Outline each blood parasite and name the species.
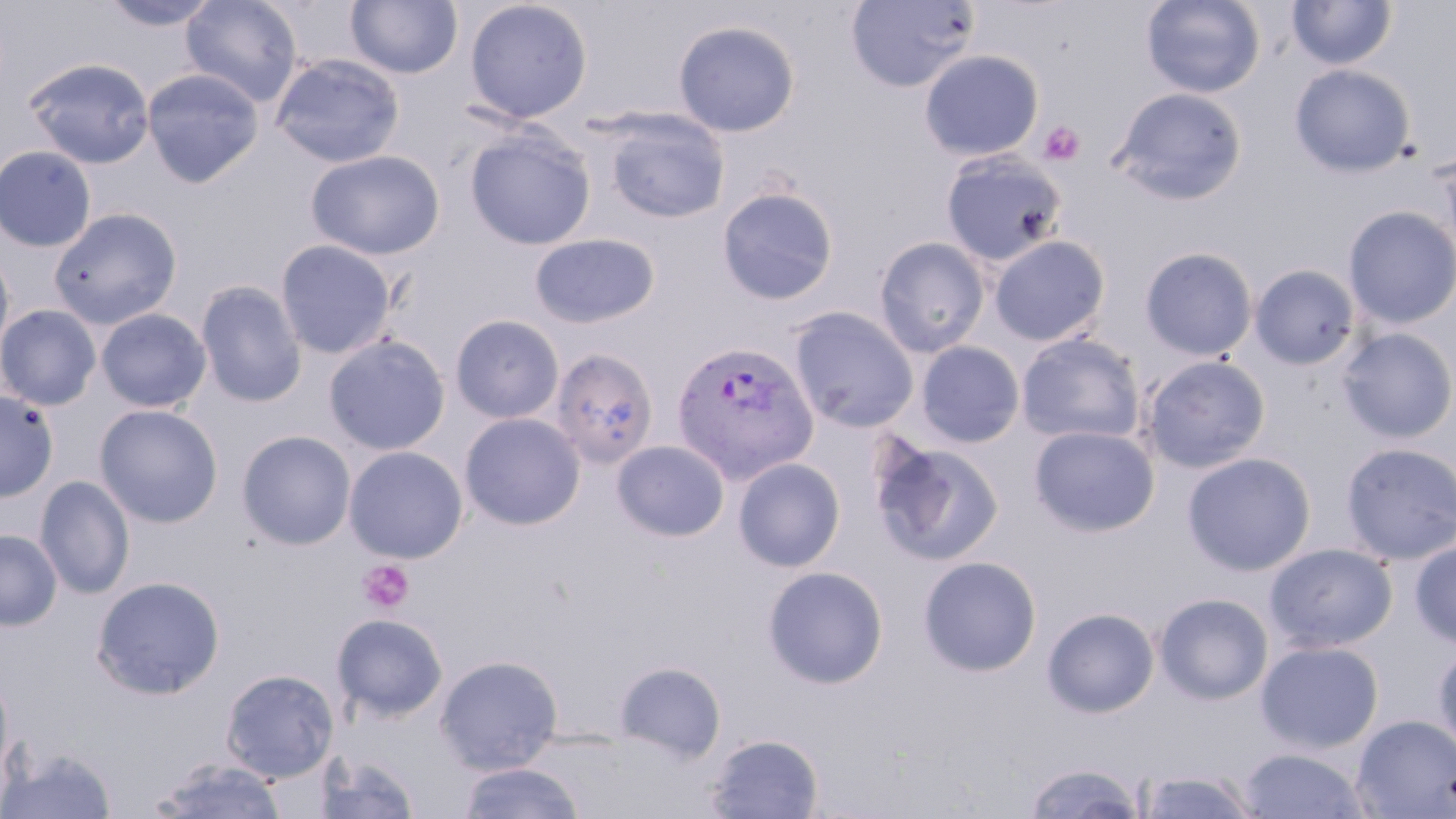
Approximate bounding boxes as [x1, y1, x2, y2] in pixels.
Plasmodium vivax-infected red blood cells: [674, 345, 821, 489].
No Plasmodium falciparum, Plasmodium ovale, Plasmodium malariae, Babesia divergens, or Trypanosoma brucei observed.

Platelet locations: [1038, 121, 1084, 167], [357, 559, 414, 613]. Uninfected red blood cell locations: [180, 0, 303, 107], [463, 0, 593, 124], [846, 0, 981, 93], [1141, 0, 1266, 98], [1286, 0, 1397, 70], [99, 1, 223, 32], [345, 1, 463, 79], [673, 20, 800, 137], [919, 49, 1044, 161], [269, 53, 405, 168], [23, 57, 156, 169], [1289, 64, 1416, 177], [141, 68, 265, 187], [1110, 87, 1248, 205], [600, 109, 729, 224], [464, 127, 596, 250], [1437, 144, 1456, 261], [0, 145, 98, 253], [306, 149, 445, 260], [940, 151, 1069, 266], [716, 186, 839, 305], [1342, 205, 1456, 329], [48, 207, 183, 329], [529, 233, 660, 329], [989, 235, 1111, 346], [873, 236, 991, 357], [275, 239, 396, 359], [0, 244, 15, 364], [1139, 247, 1258, 361], [1250, 264, 1360, 370], [195, 280, 307, 408], [0, 304, 102, 410], [788, 306, 920, 434], [95, 308, 212, 413], [449, 314, 565, 424], [1336, 327, 1456, 443], [1015, 332, 1145, 445], [322, 334, 450, 455], [915, 342, 1025, 448], [549, 348, 659, 469], [1138, 355, 1271, 473], [0, 389, 59, 502], [94, 404, 223, 527], [459, 412, 586, 530], [1029, 424, 1159, 536], [236, 430, 356, 550], [869, 437, 1005, 567], [611, 440, 730, 542], [1339, 442, 1456, 565], [343, 445, 468, 563], [1182, 451, 1317, 576], [732, 457, 846, 572], [35, 475, 135, 598], [0, 528, 62, 630], [1410, 538, 1456, 649], [1264, 543, 1398, 652], [917, 555, 1042, 676], [762, 566, 888, 689], [91, 575, 225, 699], [1153, 593, 1274, 704], [1042, 607, 1160, 718], [331, 613, 448, 722], [1256, 640, 1383, 753], [1432, 645, 1456, 758], [435, 654, 563, 774], [613, 660, 727, 763], [221, 668, 338, 782], [0, 669, 14, 790], [1353, 714, 1456, 817], [706, 733, 824, 818], [2, 746, 118, 818], [1237, 747, 1371, 818], [312, 750, 422, 819], [150, 756, 288, 819], [1022, 761, 1148, 818], [457, 762, 586, 819], [1135, 768, 1261, 817]. Slide-level diagnosis: Plasmodium vivax. Captured at 1000x magnification. One field of a larger specimen. May-Grünwald-Giemsa-stained preparation. Thin blood smear. Optical microscopy. Image is 1456×819 pixels.